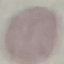

Malaria status: uninfected. Automatically extracted cell patch, resized to 64 × 64 pixels. Thin smear of blood. Giemsa-stained preparation. Photographed with a smartphone camera at the microscope eyepiece.